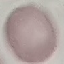
Summary:
  - Malaria status: uninfected
  - Stain: Giemsa
  - Preparation: thin smear
  - Capture: smartphone camera at the microscope eyepiece
  - Image type: cell patch, automatically extracted from a larger field of view and resized to 64 × 64 pixels